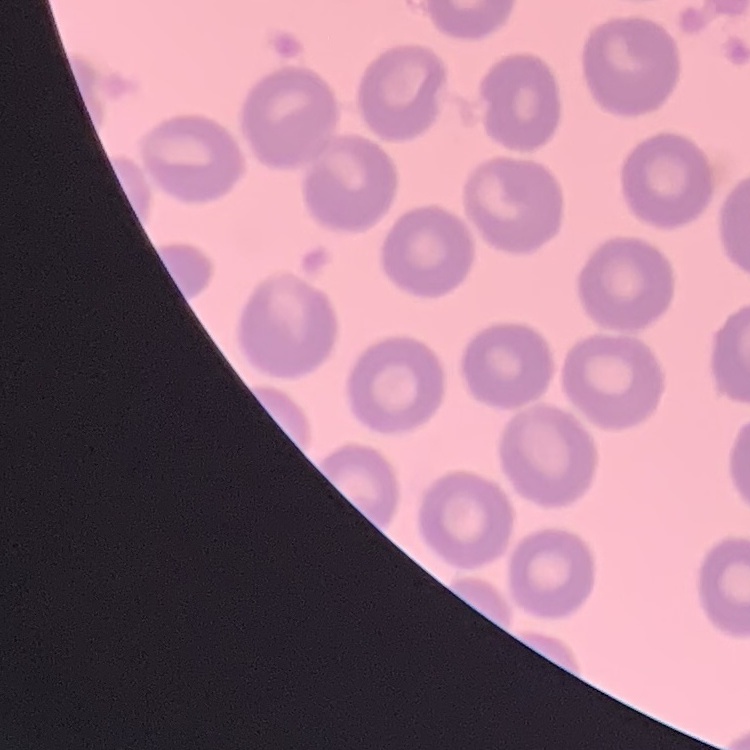
red blood cell morphology = no rouleaux formation
stain = Field's or Giemsa
preparation = thin peripheral smear
image type = square crop of a larger photomicrograph